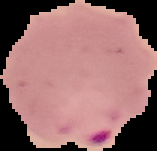

Summary:
  - Malaria status: parasitized
  - Image size: 157×151 pixels
  - Preparation: thin blood film
  - Image type: cell region segmented out of the field of view; surrounding area masked to black